Name the cell type shown.
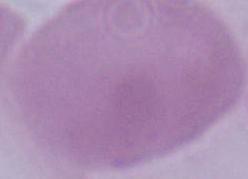

An erythrocyte.

Summary:
  - Magnification: 1000x
  - Modality: photomicrograph